Assess for malaria.
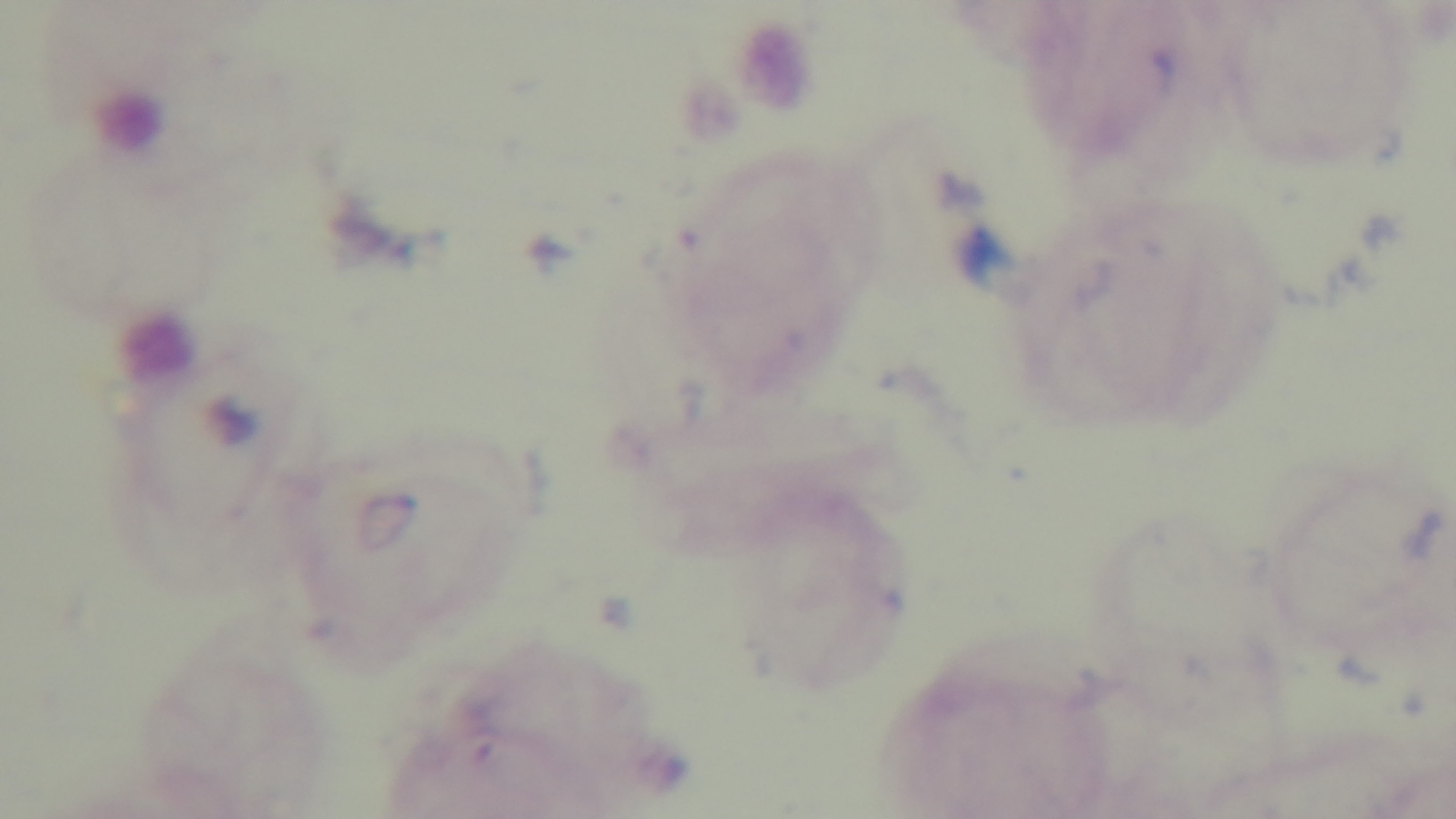
Negative.

Preparation: thick blood film. Photomicrograph. Captured with a mounted 4K digital camera. Oil-immersion objective, 100x. Single field of view. Giemsa-stained.